Report the malaria status of this cell.
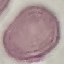

It is uninfected.

Giemsa stain. Photographed with a smartphone camera at the microscope eyepiece. Thin smear of blood. Cell patch, automatically extracted from a larger field of view and resized to 64 × 64 pixels.